Report the malaria status of this cell.
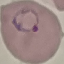

Parasitized.

preparation = thin blood film
capture = smartphone through the microscope eyepiece
stain = Giemsa
image type = cell patch, automatically extracted from a larger field of view and resized to 64 × 64 pixels